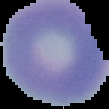
Summary:
  - Preparation: thin blood film
  - Image type: segmented cell region on a black background
  - Result: no malaria parasites detected
  - Image size: 109×109 pixels